Classify this cell by malaria status.
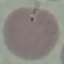

Uninfected.

capture = smartphone through the microscope eyepiece
preparation = thin smear
stain = Giemsa
image type = automatically extracted cell patch, resized to 64 × 64 pixels